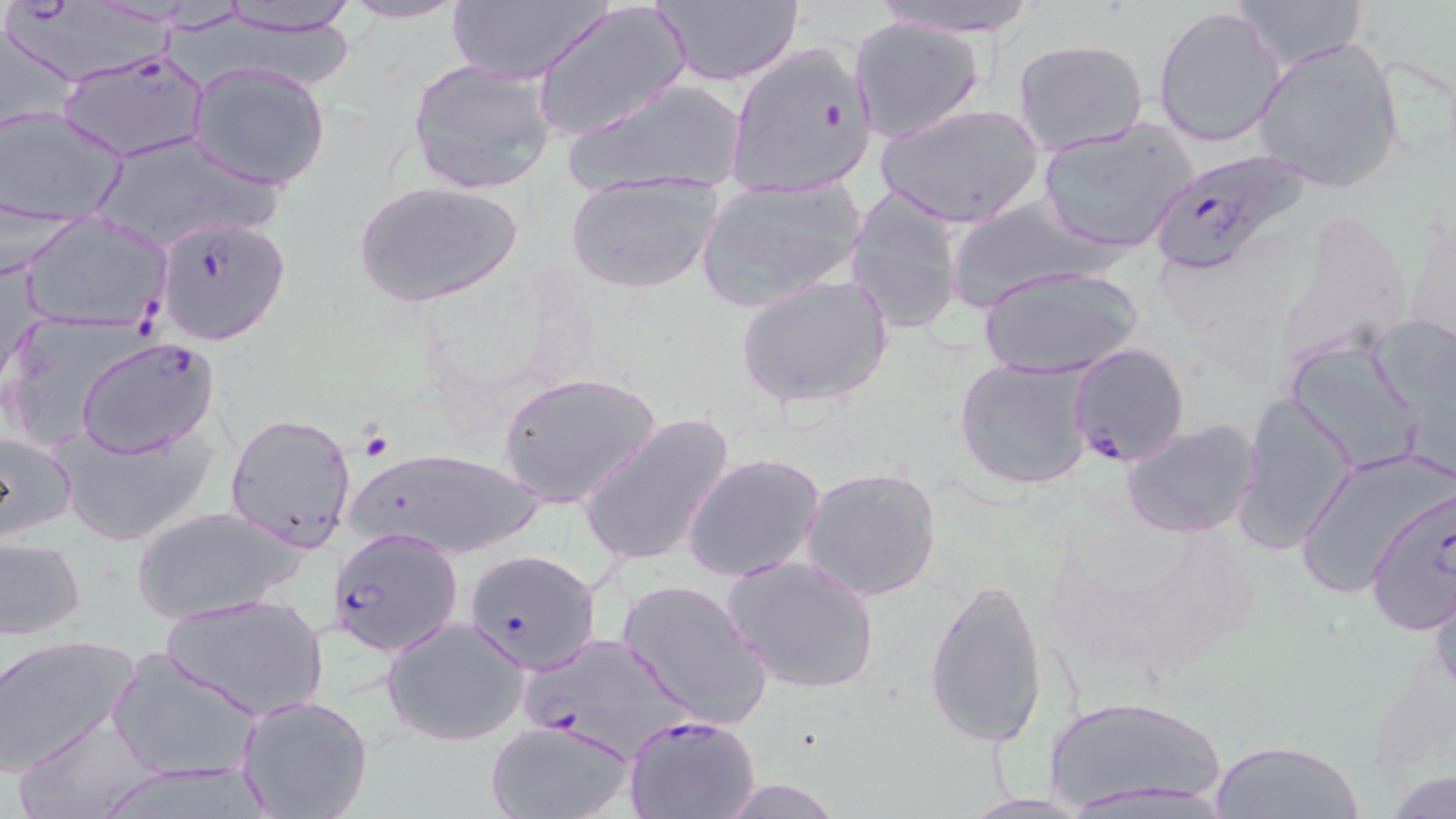

Approximate bounding boxes as (x1, y1, x2, y2) in pixels. Uninfected red blood cell locations: (339, 0, 471, 24), (647, 0, 805, 88), (863, 0, 1051, 40), (1226, 0, 1367, 70), (203, 1, 360, 38), (443, 1, 612, 84), (532, 1, 689, 143), (1153, 5, 1286, 149), (2, 15, 84, 142), (849, 18, 984, 142), (1251, 36, 1406, 195), (1013, 38, 1148, 153), (407, 60, 558, 195), (187, 62, 334, 190), (563, 76, 749, 199), (876, 103, 1045, 228), (1, 104, 129, 230), (1036, 119, 1197, 254), (89, 131, 283, 253), (566, 173, 720, 295), (696, 178, 863, 310), (352, 179, 525, 308), (844, 186, 965, 335), (943, 194, 1109, 309), (1278, 206, 1418, 373), (18, 211, 174, 333), (1404, 213, 1455, 353), (978, 264, 1146, 381), (735, 273, 894, 410), (1367, 310, 1456, 462), (0, 311, 144, 450), (1284, 338, 1427, 474), (954, 356, 1096, 491), (497, 371, 663, 511), (1235, 391, 1360, 555), (225, 411, 357, 549), (577, 413, 737, 569), (1121, 418, 1262, 538), (54, 420, 217, 549), (0, 427, 78, 543), (344, 444, 546, 561), (1295, 449, 1453, 603), (682, 452, 826, 584), (801, 464, 943, 602), (128, 504, 311, 624), (1, 537, 86, 641), (722, 552, 881, 695), (1424, 572, 1456, 696), (923, 574, 1048, 750), (617, 577, 774, 730), (161, 592, 329, 722), (382, 616, 530, 746), (0, 636, 140, 778), (109, 647, 262, 784), (236, 693, 374, 818), (1039, 693, 1230, 815), (14, 710, 162, 819), (485, 717, 636, 819), (1210, 736, 1365, 818), (1382, 768, 1456, 818), (1065, 777, 1231, 815), (707, 779, 850, 817), (958, 792, 1099, 818). Plasmodium falciparum-infected red blood cell locations: (722, 41, 885, 202), (56, 47, 211, 164), (1147, 146, 1314, 277), (154, 214, 292, 345), (75, 337, 222, 460), (1066, 340, 1190, 468), (1365, 486, 1456, 636), (326, 527, 460, 655), (464, 550, 600, 673), (524, 632, 694, 759), (623, 714, 762, 819). Slide-level diagnosis: Plasmodium falciparum. Image is 1456×819 pixels. Light microscopy. May-Grünwald-Giemsa-stained preparation. Thin blood smear. One field of a larger specimen. Captured at 1000x magnification.